Classify this cell by malaria status.
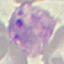
Parasitized.

stain: Giemsa
capture: smartphone camera at the microscope eyepiece
preparation: thin smear
image_type: cell patch, automatically extracted from a larger field of view and resized to 64 × 64 pixels